State which parasite is depicted.
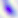

Toxoplasma gondii.

modality = photomicrograph
magnification = 400x